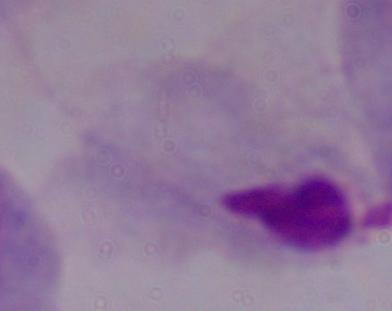

identification: trichomonad
magnification: 1000x
modality: micrograph